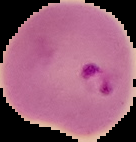

Result: Plasmodium parasites identified. Image is 136×142 pixels. From a thin blood film. The area outside the segmented cell region is set to black.